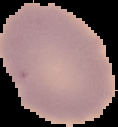

Image is 118×127 pixels. Result: no Plasmodium parasites seen. From a thin blood film. The area outside the segmented cell region is set to black.